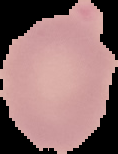

image size = 118×154 pixels
preparation = thin blood film
image type = cell region segmented out of the field of view; surrounding area masked to black
malaria status = uninfected